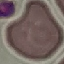
Summary:
  - Result: no malaria parasites detected
  - Image type: cell patch, automatically extracted from a larger field of view and resized to 64 × 64 pixels
  - Preparation: thin blood smear
  - Stain: Giemsa
  - Capture: smartphone through the microscope eyepiece